Assess this cell for malaria.
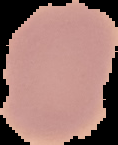
Uninfected.

Summary:
  - Image type: segmented cell region with the area outside set to black
  - Image size: 118×145 pixels
  - Preparation: thin blood film